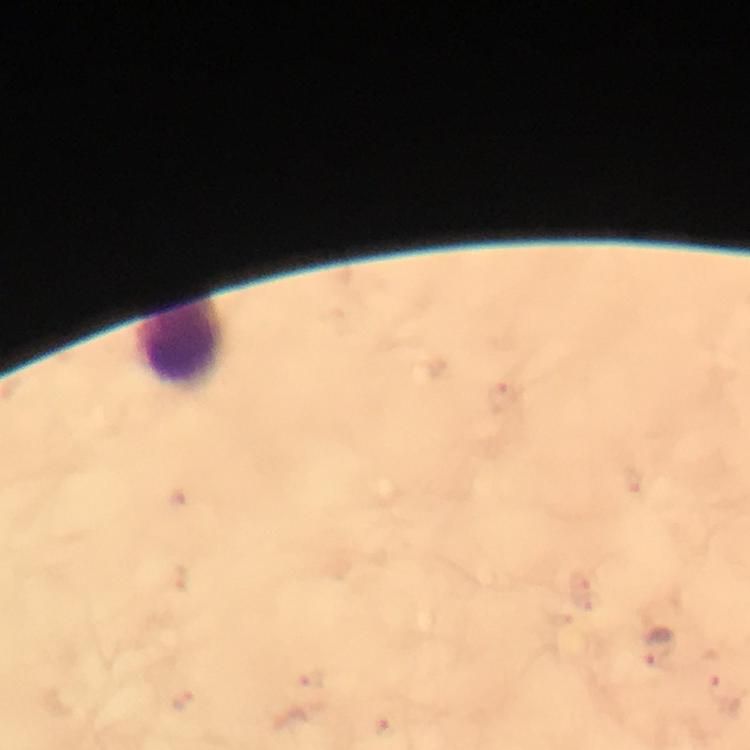 Approximate centers as (x, y) in pixels. Plasmodium parasite locations: (659, 647). Leukocyte locations: (183, 347). A crop from one field of view. Thick smear. Image is 750×750 pixels. Giemsa stain. 100x magnification. From a diagnostic examination for malaria. Immersion oil was used. Smartphone photograph taken through a microscope.